Report the malaria status of this cell.
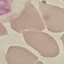

Uninfected.

image type = cell patch, automatically extracted from a larger field of view and resized to 64 × 64 pixels
capture = smartphone camera at the microscope eyepiece
stain = Giemsa
preparation = thin blood film